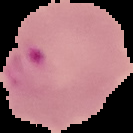

Cell region segmented out of the field of view; the surrounding area is masked to black. Image is 133×133 pixels. Malaria status: parasitized. From a thin blood film.